Classify this cell by malaria status.
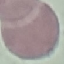

It is uninfected.

Giemsa-stained preparation. Cell patch, automatically extracted from a larger field of view and resized to 64 × 64 pixels. Thin blood film. Photographed with a smartphone camera at the microscope eyepiece.